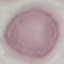 Result: no malaria parasites detected. Photographed with a smartphone camera at the microscope eyepiece. Giemsa-stained preparation. Automatically extracted cell patch, resized to 64 × 64 pixels. Thin blood film.